Give the position of every Plasmodium parasite visible.
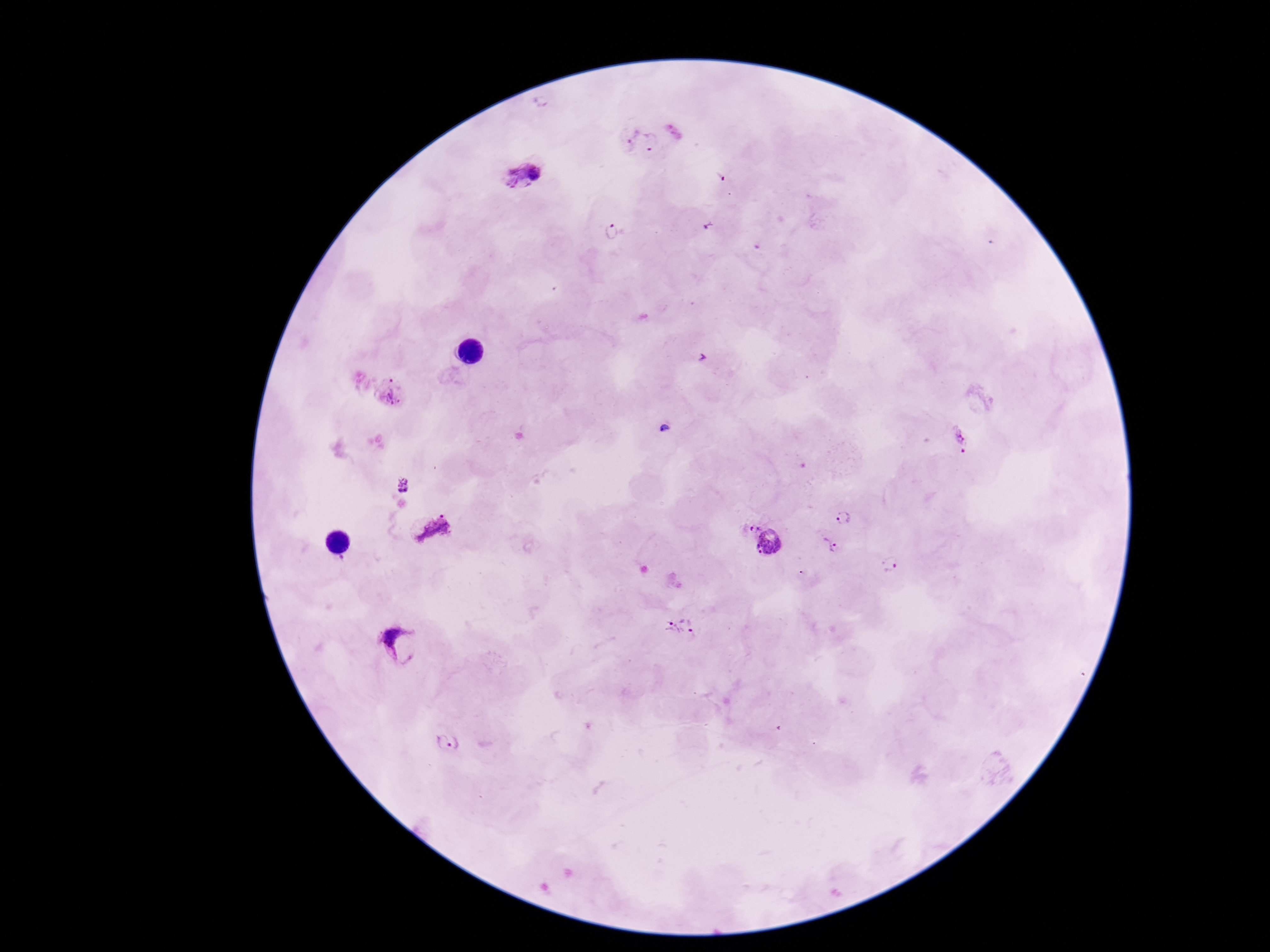

Approximate centers as {x, y} in pixels.
Plasmodium parasites: {630, 134}, {652, 142}, {522, 176}, {611, 232}, {391, 393}, {665, 429}, {961, 438}, {403, 487}, {842, 518}, {748, 526}, {434, 530}, {771, 544}, {827, 544}, {890, 564}, {683, 627}, {404, 646}, {447, 747}.

Image is 1270×952 pixels. Photographed through the microscope eyepiece with a smartphone camera. 100x magnification. Giemsa-stained preparation. Thick blood smear. Patient malaria status: positive. Single field of view.